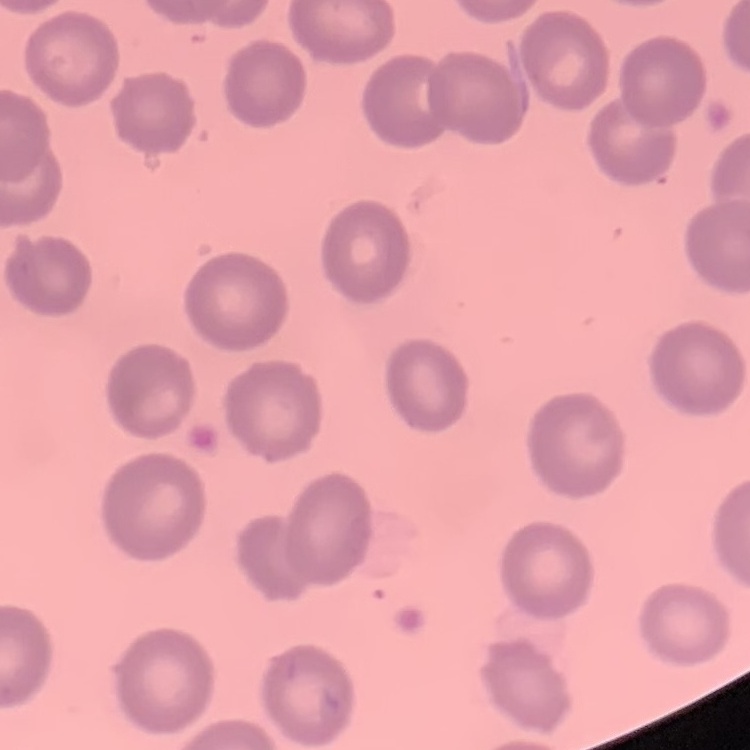
Summary:
  - Erythrocyte morphology: no rouleaux formation
  - Image type: square crop of a larger photomicrograph
  - Stain: Field's or Giemsa
  - Preparation: thin blood film